Locate every Plasmodium parasite.
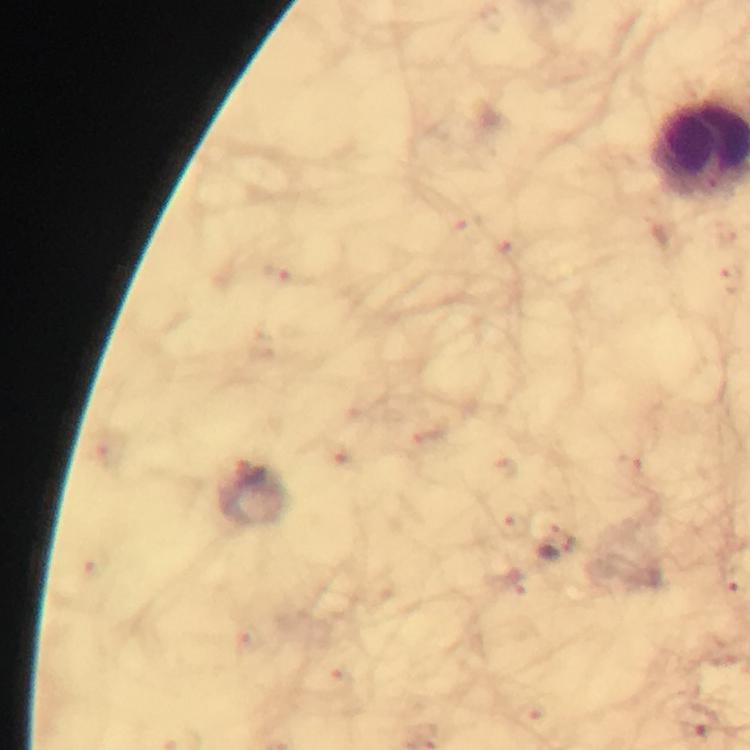

Approximate centers as {x, y} in pixels.
Plasmodium parasites: {556, 548}.

Photographed with a smartphone mounted on the microscope. Image is 750×750 pixels. A crop from one field of view. Thick blood film. Giemsa-stained preparation. At 100x magnification. Immersion oil was used. From a malaria diagnostic workup.